Name the parasite shown.
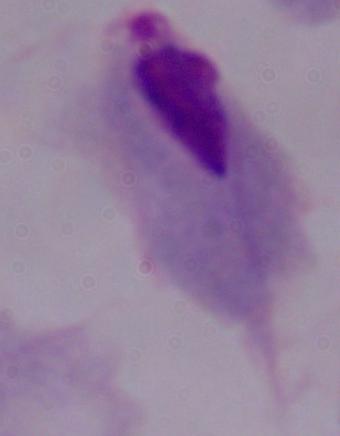
This is a trichomonad.

Summary:
  - Modality: micrograph
  - Magnification: 1000x